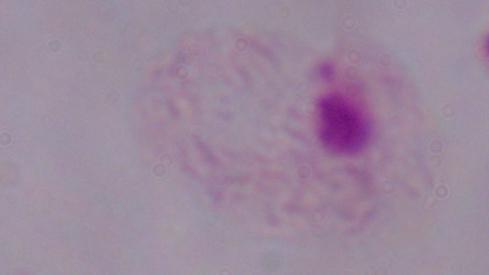

Micrograph. 1000x magnification. A trichomonad is shown.